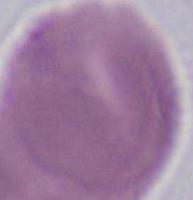
magnification: 1000x
identification: red blood cell
modality: photomicrograph